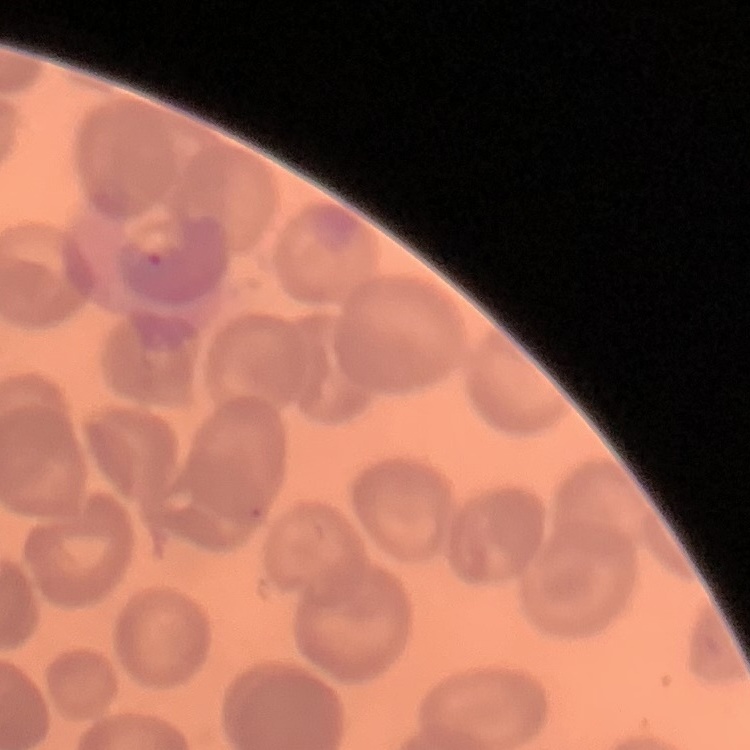 The red blood cells exhibit no rouleaux formation. One tile cut from a larger photomicrograph. Field's or Giemsa stain. Thin blood smear.